Classify this cell by malaria status.
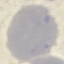
It is uninfected.

Thin smear of blood. Giemsa-stained preparation. Cell patch, automatically extracted from a larger field of view and resized to 64 × 64 pixels. Acquired by smartphone through the microscope eyepiece.